Locate every leukocyte (white blood cell).
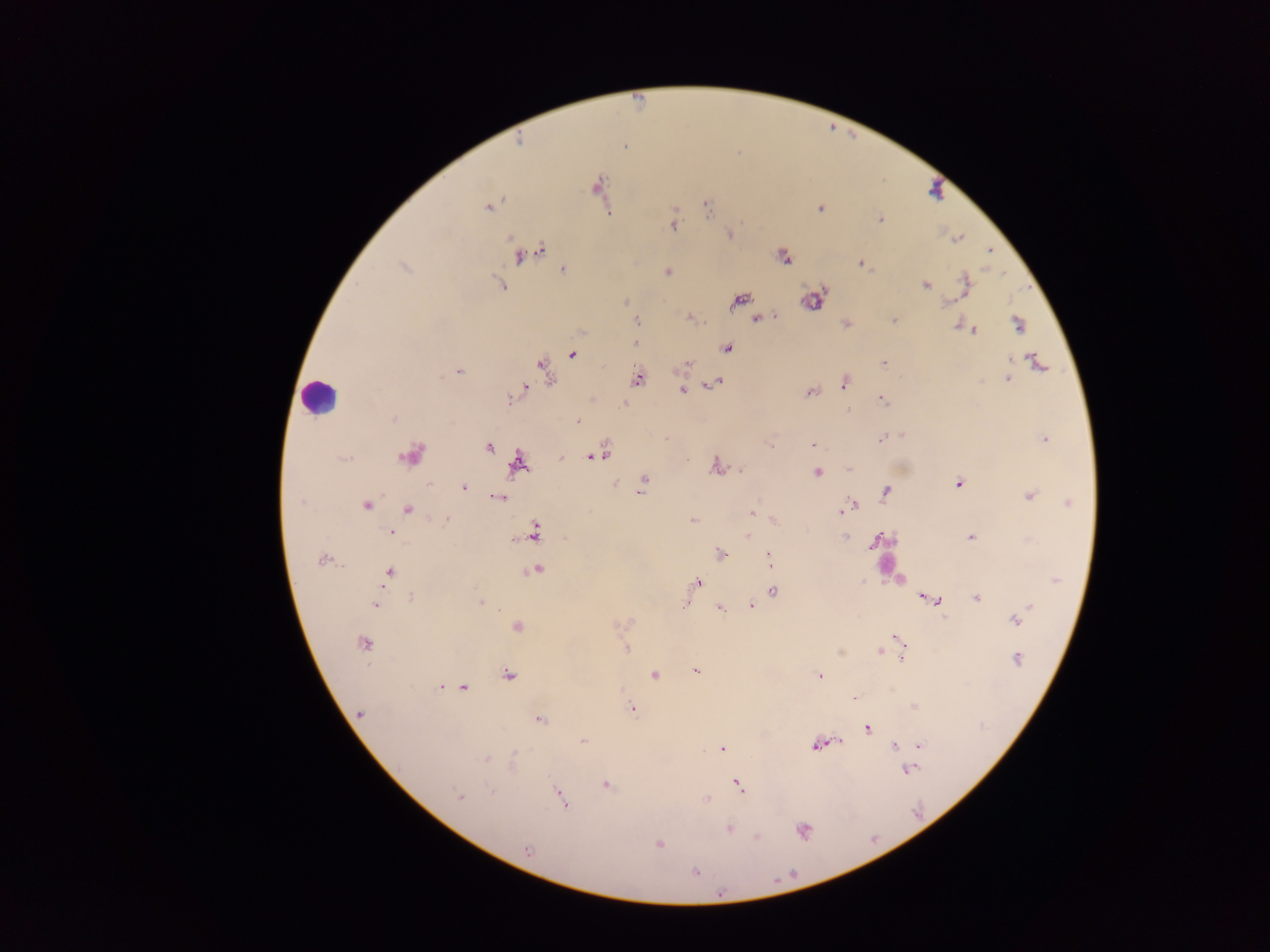
Approximate centers as [x, y] in pixels.
Leukocytes: [935, 190], [319, 395].

Malaria parasite locations: [624, 146], [597, 186], [488, 206], [706, 207], [820, 208], [880, 220], [673, 225], [729, 234], [958, 239], [990, 250], [528, 251], [784, 257], [862, 263], [405, 267], [564, 270], [667, 272], [965, 284], [501, 285], [925, 286], [740, 300], [813, 300], [626, 302], [949, 302], [761, 318], [894, 319], [636, 321], [846, 324], [958, 325], [1019, 326], [974, 330], [636, 343], [728, 348], [572, 355], [1010, 359], [1038, 362], [686, 364], [884, 364], [545, 369], [459, 371], [1008, 378], [638, 379], [716, 381], [979, 382], [845, 383], [522, 390], [683, 390], [810, 393], [516, 394], [882, 399], [624, 403], [847, 410], [393, 419], [578, 421], [901, 434], [881, 439], [1044, 439], [812, 444], [770, 445], [488, 447], [601, 453], [411, 455], [593, 456], [343, 459], [517, 464], [715, 466], [741, 469], [849, 469], [817, 473], [644, 480], [614, 483], [958, 484], [463, 487], [641, 491], [886, 492], [1030, 496], [499, 497], [301, 502], [1069, 503], [367, 506], [849, 506], [408, 509], [841, 511], [752, 513], [446, 520], [775, 520], [693, 521], [390, 532], [534, 532], [748, 536], [844, 538], [971, 538], [873, 543], [720, 554], [769, 557], [322, 559], [536, 570], [389, 573], [1056, 580], [697, 582], [862, 582], [774, 592], [977, 597], [410, 598], [929, 599], [480, 602], [941, 604], [376, 605], [751, 605], [1029, 606], [683, 607], [720, 608], [1022, 613], [1015, 620], [517, 627], [899, 639], [364, 643], [627, 649], [901, 649], [879, 651], [902, 658], [1017, 660], [696, 671], [508, 675], [654, 675], [820, 675], [440, 687], [463, 688], [854, 698], [914, 706], [632, 708], [359, 714], [540, 720], [868, 729], [584, 740], [839, 740], [815, 746], [894, 746], [921, 746], [722, 749], [486, 760], [513, 761], [908, 771], [605, 785], [737, 785], [490, 791], [458, 796], [560, 797], [705, 799], [729, 829], [803, 830], [757, 837], [659, 844], [527, 849], [696, 872], [720, 894]. Thick blood film. Image is 1270×952 pixels. Single field of view. Collected in Ghana. Photographed through a microscope with a mobile-phone camera.